Give the position of every Plasmodium parasite visible.
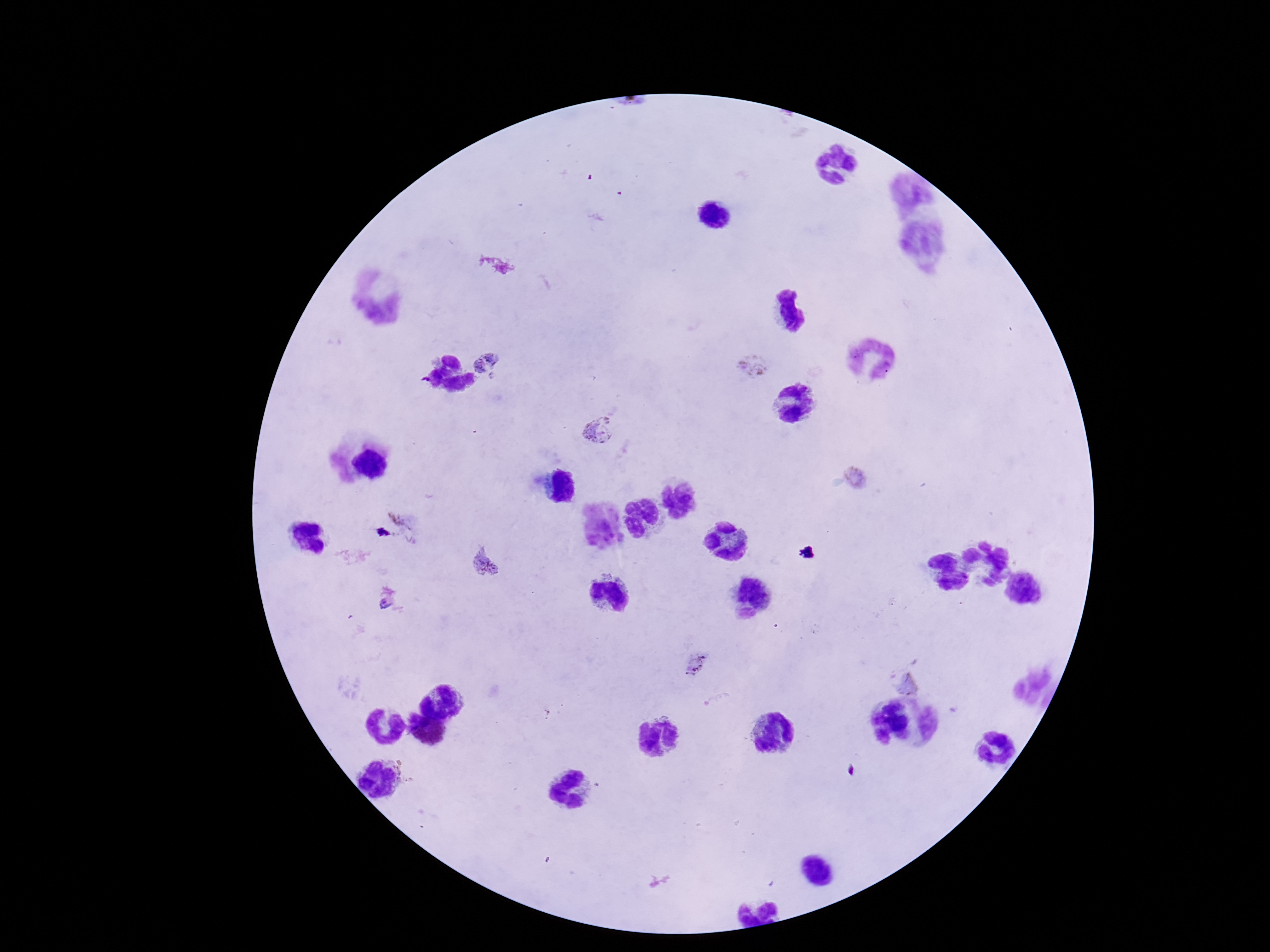
Approximate centers as [x, y] in pixels.
Plasmodium parasites: [489, 363], [753, 367], [602, 428], [856, 479], [414, 525], [484, 562], [384, 605], [699, 665], [908, 681].

Patient malaria status: infected. Photographed through the microscope eyepiece with a smartphone camera. Image is 1270×952 pixels. 100x magnification. Thick peripheral-blood smear. Giemsa-stained preparation. Single field of view.